Report the malaria status of this cell.
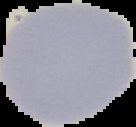

It is uninfected.

The area outside the segmented cell region is set to black. From a thin blood film. Image is 136×127 pixels.